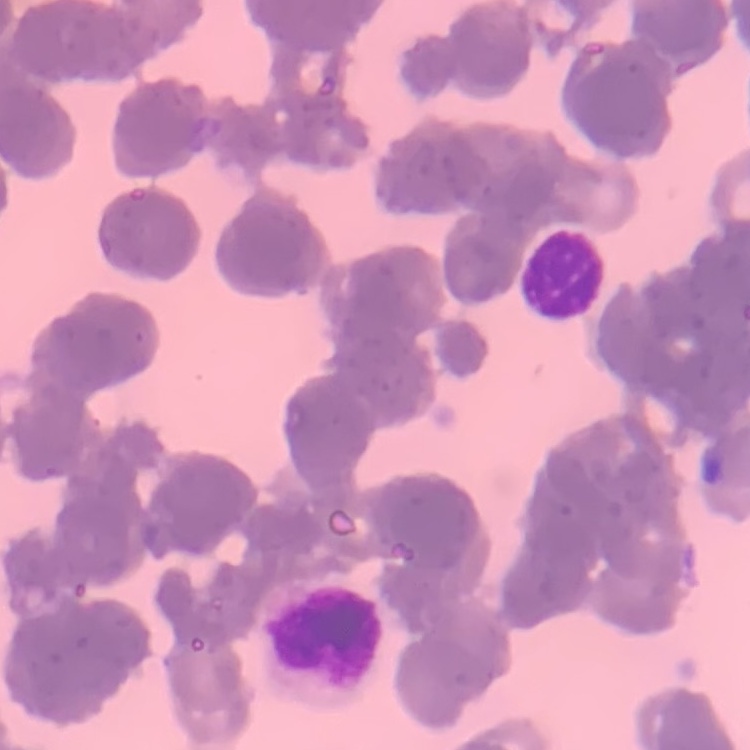
erythrocyte morphology = rouleaux formation
preparation = thin blood film
stain = Field's or Giemsa
image type = square crop of a larger photomicrograph